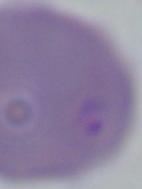 A Babesia parasite is seen. Micrograph. 1000x magnification.